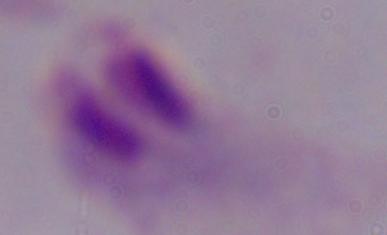 Photomicrograph. A trichomonad is seen. 1000x magnification.